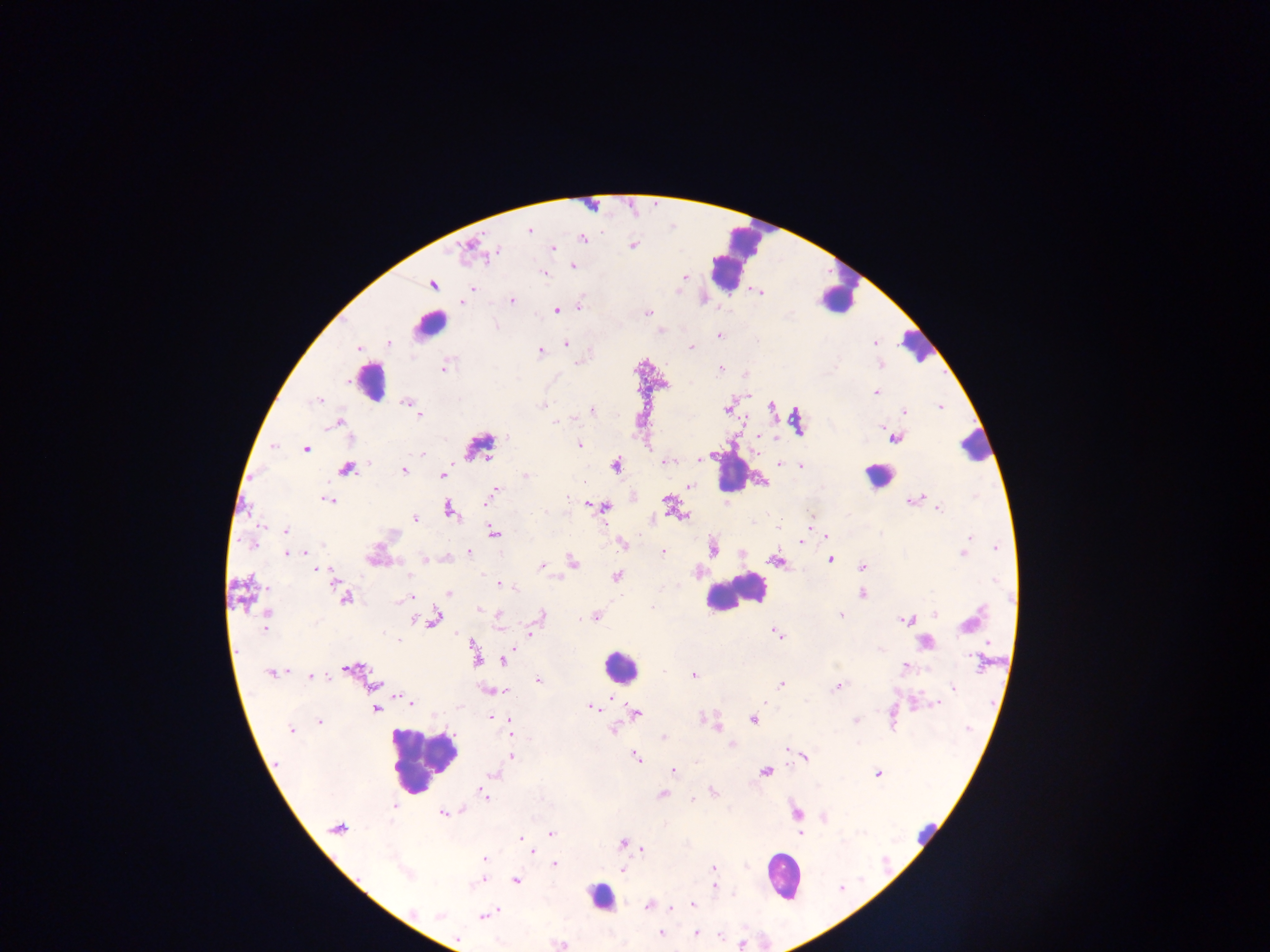

Approximate centers as x y in pixels. Leukocyte locations: 734 259; 839 296; 429 324; 916 346; 369 380; 975 447; 732 472; 876 475; 733 593; 619 666; 422 760; 926 829; 782 876; 600 897. Malaria parasite locations: 529 230; 583 238; 633 245; 553 248; 496 251; 573 267; 543 274; 684 276; 433 285; 472 288; 761 293; 512 300; 462 303; 579 305; 556 311; 648 312; 719 335; 389 343; 565 343; 874 343; 691 347; 358 350; 540 351; 721 367; 444 368; 876 393; 318 399; 405 402; 543 405; 939 406; 771 407; 415 410; 727 410; 591 411; 904 411; 420 415; 556 422; 337 424; 882 427; 506 437; 760 437; 897 439; 579 444; 273 446; 306 449; 422 453; 699 460; 667 462; 781 463; 616 465; 801 466; 346 469; 404 470; 442 475; 525 476; 689 486; 496 490; 492 495; 567 497; 923 497; 918 499; 328 500; 487 501; 910 501; 667 502; 605 507; 938 509; 449 510; 544 513; 681 516; 415 518; 779 529; 285 531; 494 532; 826 537; 969 537; 801 541; 623 543; 252 544; 321 545; 997 548; 713 549; 469 552; 287 553; 662 553; 964 553; 425 559; 830 559; 774 561; 572 562; 541 566; 863 566; 315 569; 408 576; 617 577; 995 580; 332 581; 500 584; 514 588; 448 593; 862 594; 410 597; 346 599; 404 599; 652 607; 480 610; 494 611; 267 612; 935 613; 498 615; 541 616; 840 616; 597 617; 581 619; 266 620; 434 620; 905 620; 970 624; 264 628; 777 632; 531 634; 399 640; 925 642; 476 656; 976 660; 505 662; 904 667; 351 668; 663 671; 271 673; 694 675; 311 676; 538 681; 781 683; 374 684; 838 687; 953 687; 504 692; 612 699; 411 702; 937 704; 591 707; 376 708; 636 714; 491 717; 704 718; 752 719; 510 720; 319 721; 856 721; 511 729; 613 729; 290 730; 663 737; 788 749; 511 755; 805 756; 636 758; 673 770; 765 771; 877 774; 493 775; 713 791; 483 794; 663 795; 697 796; 692 799; 394 806; 462 810; 442 813; 824 818; 337 828; 800 833; 551 834; 520 839; 622 843; 642 849; 532 850; 484 859; 554 864; 713 868; 623 871; 480 881; 515 881; 714 887; 648 905; 693 905; 671 908; 413 912; 490 912; 439 915; 485 915; 661 934; 696 934; 720 936; 457 939; 741 945. Image is 1270×952 pixels. Sample from Ghana. Single field of view. Thick blood film. Mobile-phone photograph taken through the microscope.